Point out each malaria parasite.
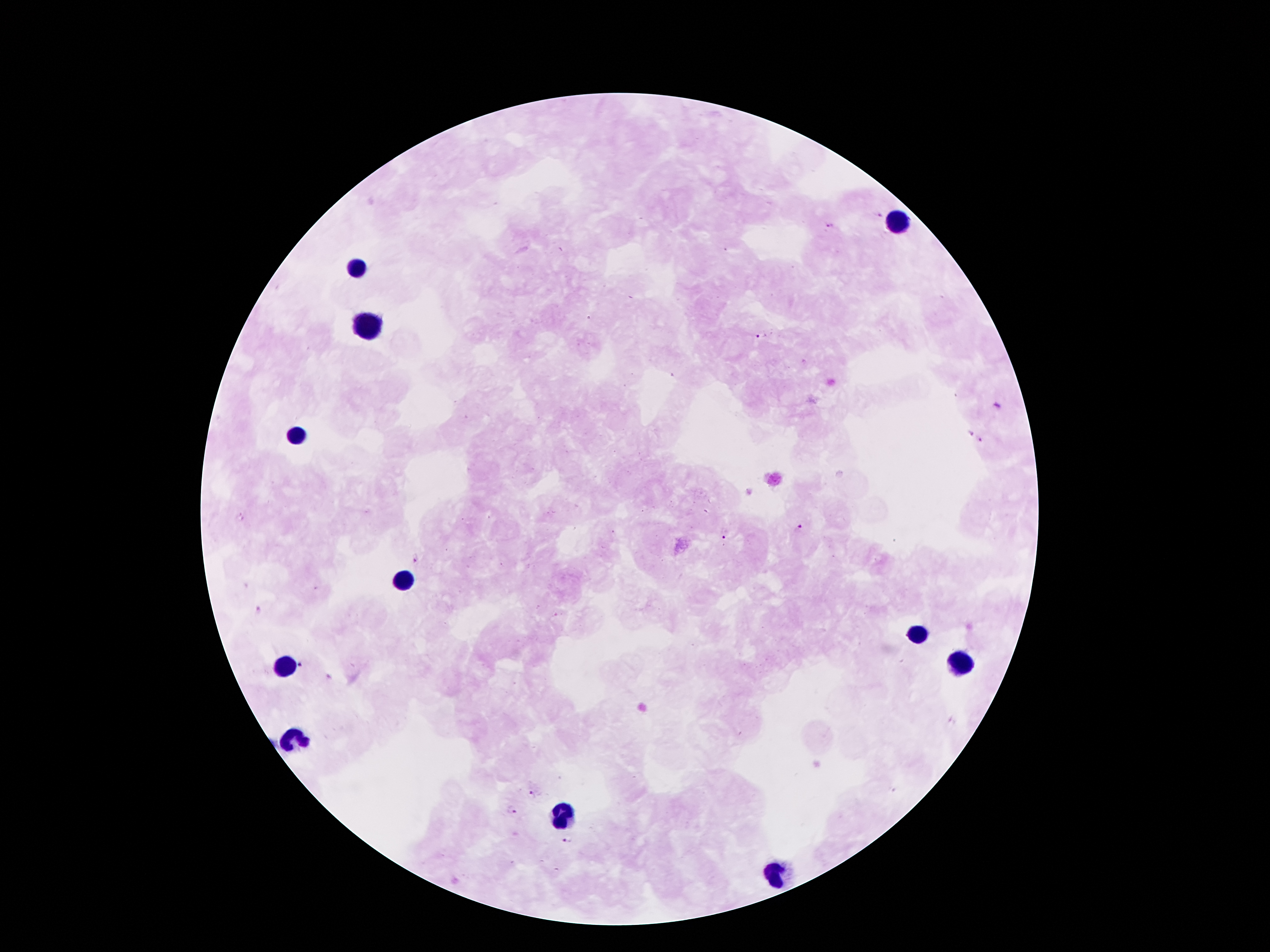

Approximate centers as [x, y] in pixels.
Malaria parasites: [877, 216], [828, 227], [755, 337], [999, 407], [971, 434], [981, 442], [798, 529], [725, 538], [416, 560], [260, 610], [303, 666], [532, 794], [511, 811], [569, 840].

{
  "field_of_view": "single",
  "preparation": "thick peripheral-blood smear",
  "stain": "Giemsa",
  "patient_malaria_status": "positive for Plasmodium falciparum",
  "capture": "smartphone through the microscope eyepiece",
  "leukocyte_locations": "approximate centers as [x, y] in pixels: [899, 223], [359, 269], [368, 320], [297, 435], [399, 578], [912, 636], [958, 665], [284, 667], [295, 738], [560, 813], [777, 873]",
  "image_size": "1270×952 pixels",
  "magnification": "100x"
}